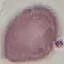

Summary:
  - Malaria status: uninfected
  - Image type: automatically extracted cell patch, resized to 64 × 64 pixels
  - Stain: Giemsa
  - Preparation: thin blood film
  - Capture: smartphone through the microscope eyepiece